Classify this cell by malaria status.
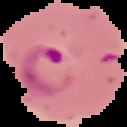
Parasitized.

Segmented cell region on a black background. From a thin blood smear. Image is 127×127 pixels.